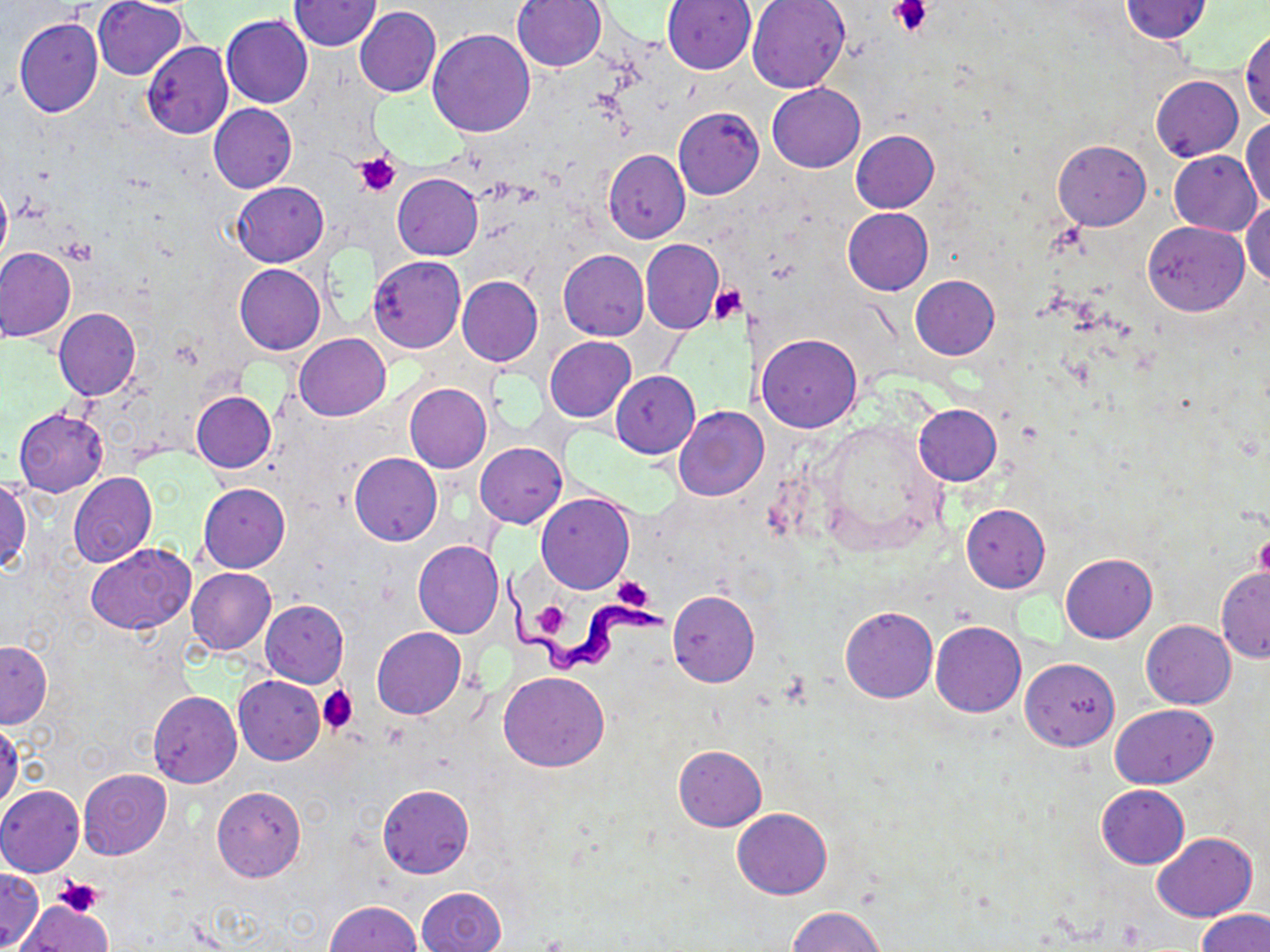

Approximate bounding boxes as (x1, y1, x2, y2) in pixels. Platelet locations: (889, 0, 932, 37), (353, 151, 401, 197), (708, 284, 747, 324), (1255, 533, 1270, 584), (611, 577, 655, 612), (530, 601, 573, 640), (317, 685, 358, 735), (53, 877, 103, 916), (31, 896, 112, 945). Uninfected red blood cell locations: (92, 0, 188, 80), (748, 0, 850, 93), (1121, 0, 1212, 44), (288, 1, 381, 50), (513, 1, 607, 72), (661, 1, 756, 74), (354, 6, 440, 97), (221, 15, 313, 108), (14, 18, 103, 118), (1241, 28, 1269, 121), (428, 30, 535, 137), (141, 42, 233, 139), (1151, 74, 1242, 161), (766, 83, 865, 172), (209, 104, 296, 192), (674, 107, 764, 200), (1242, 119, 1269, 211), (851, 129, 939, 212), (1052, 140, 1150, 230), (603, 149, 689, 243), (1169, 150, 1262, 236), (392, 173, 483, 259), (0, 178, 11, 272), (232, 182, 329, 267), (1243, 199, 1270, 287), (843, 207, 933, 295), (1143, 220, 1249, 316), (640, 239, 723, 333), (1, 246, 76, 342), (559, 250, 649, 340), (369, 256, 465, 353), (234, 264, 326, 355), (911, 274, 999, 359), (457, 276, 542, 368), (54, 308, 141, 401), (294, 333, 390, 420), (757, 333, 862, 431), (544, 337, 636, 422), (612, 371, 699, 457), (404, 384, 491, 472), (191, 392, 275, 473), (913, 403, 1001, 485), (673, 405, 764, 502), (14, 408, 108, 495), (475, 442, 566, 528), (349, 453, 442, 545), (67, 472, 157, 567), (0, 479, 32, 575), (198, 483, 289, 573), (537, 492, 634, 594), (960, 503, 1049, 593), (413, 541, 505, 638), (86, 543, 196, 634), (1060, 553, 1156, 643), (186, 567, 276, 655), (1216, 568, 1270, 662), (668, 590, 759, 687), (260, 600, 349, 687), (841, 605, 936, 702), (1141, 620, 1236, 708), (931, 621, 1026, 717), (372, 627, 467, 719), (1, 641, 51, 728), (1021, 658, 1119, 750), (500, 671, 608, 771), (234, 674, 325, 764), (148, 691, 241, 788), (1111, 703, 1216, 788), (0, 720, 23, 812), (673, 744, 766, 831), (78, 768, 172, 859), (378, 784, 473, 878), (0, 785, 85, 876), (212, 786, 305, 883), (1096, 786, 1189, 868), (732, 808, 833, 898), (1152, 832, 1257, 921), (0, 869, 43, 950), (417, 886, 506, 952), (18, 900, 112, 951), (327, 900, 423, 952), (788, 906, 883, 952), (1198, 910, 1270, 952). Trypanosoma brucei locations: (500, 568, 667, 677). Slide-level diagnosis: Trypanosoma brucei. Image is 1270×952 pixels. May-Grünwald-Giemsa-stained preparation. 1000x magnification. Single field of view. Light microscopy. Thin blood smear.